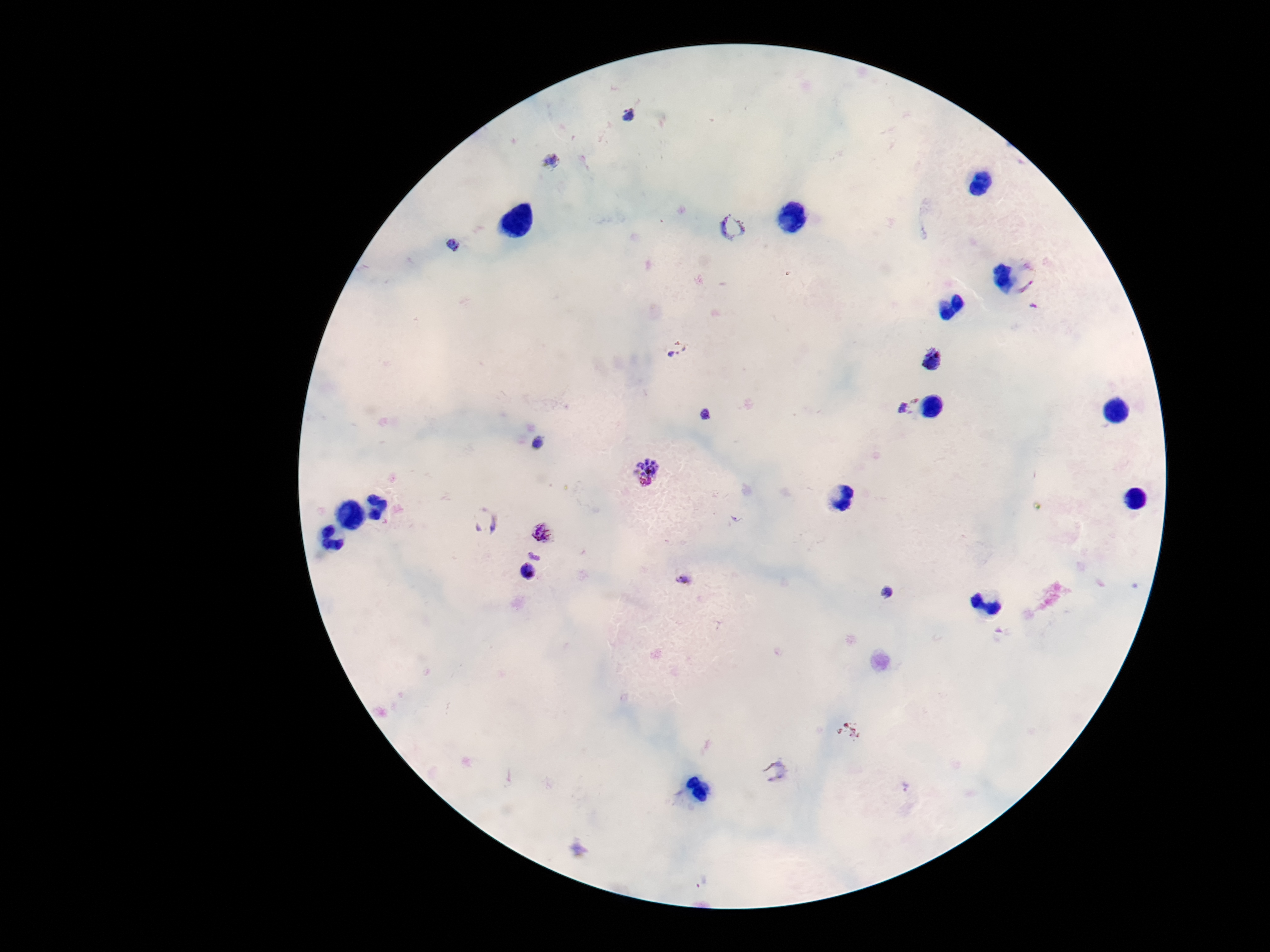

Approximate object centers, in pixels from the top-left corner.
Summary:
  - Plasmodium parasite locations: (x=628, y=116), (x=551, y=163), (x=732, y=227), (x=455, y=244), (x=1026, y=278), (x=1034, y=307), (x=675, y=348), (x=932, y=360), (x=907, y=405), (x=707, y=414), (x=538, y=444), (x=647, y=466), (x=645, y=483), (x=485, y=520), (x=543, y=532), (x=535, y=556), (x=527, y=572), (x=683, y=579), (x=887, y=593), (x=776, y=772), (x=904, y=787), (x=577, y=850), (x=701, y=882)
  - Image size: 1270×952 pixels
  - Capture: smartphone camera through the microscope eyepiece
  - Magnification: 100x
  - Field of view: one from this slide
  - Patient malaria status: infected
  - Stain: Giemsa
  - Preparation: thick blood smear